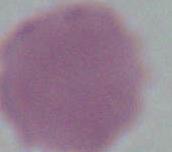
Summary:
  - Magnification: 1000x
  - Identification: erythrocyte
  - Modality: photomicrograph